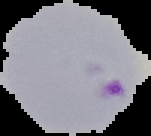

malaria status = parasitized
image size = 151×136 pixels
image type = segmented cell region on a black background
preparation = thin blood smear